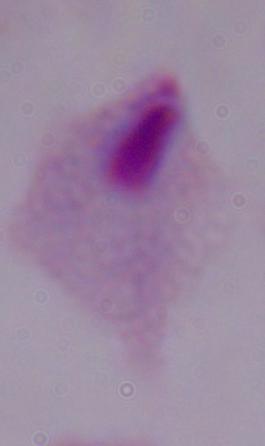
magnification = 1000x
identification = trichomonad
modality = micrograph